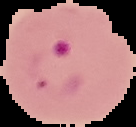
preparation = thin blood film
result = malaria parasites detected
image size = 136×127 pixels
image type = segmented cell region on a black background